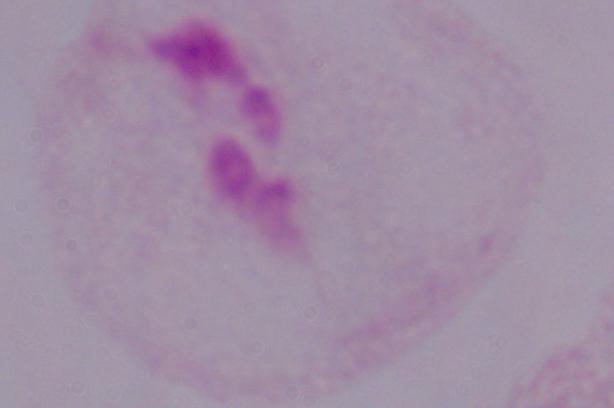 Micrograph. A trichomonad is shown. Captured at 1000x magnification.